Report the malaria status.
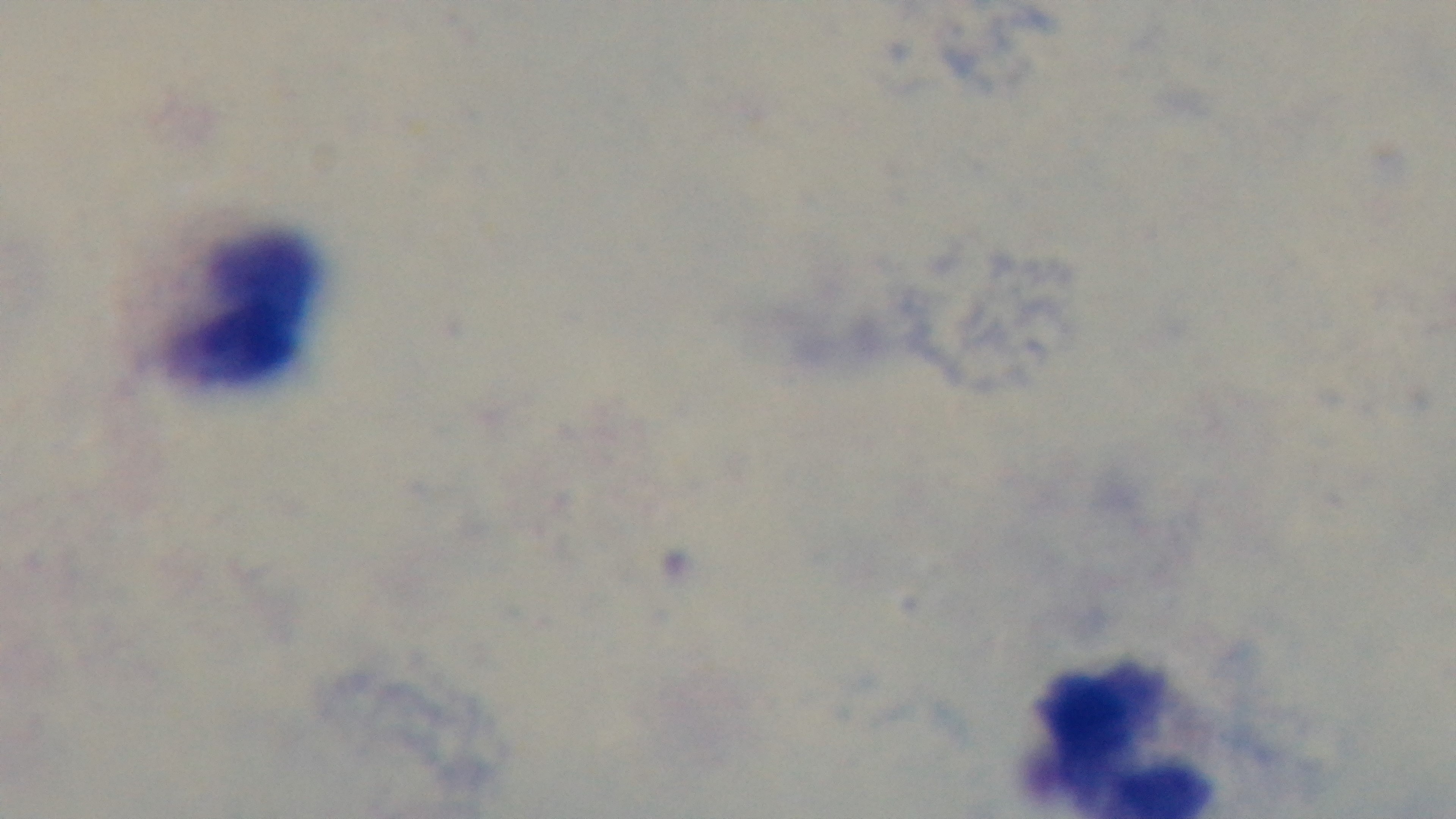
It is uninfected.

Summary:
  - Stain: Giemsa
  - Preparation: thick smear
  - Field of view: single
  - Modality: light microscopy
  - Capture: mounted 4K digital camera
  - Objective: 100x oil immersion